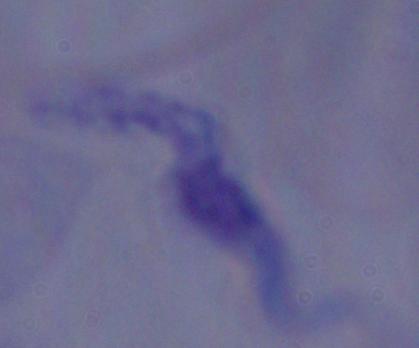
Summary:
  - Identification: trypanosome
  - Modality: photomicrograph
  - Magnification: 1000x